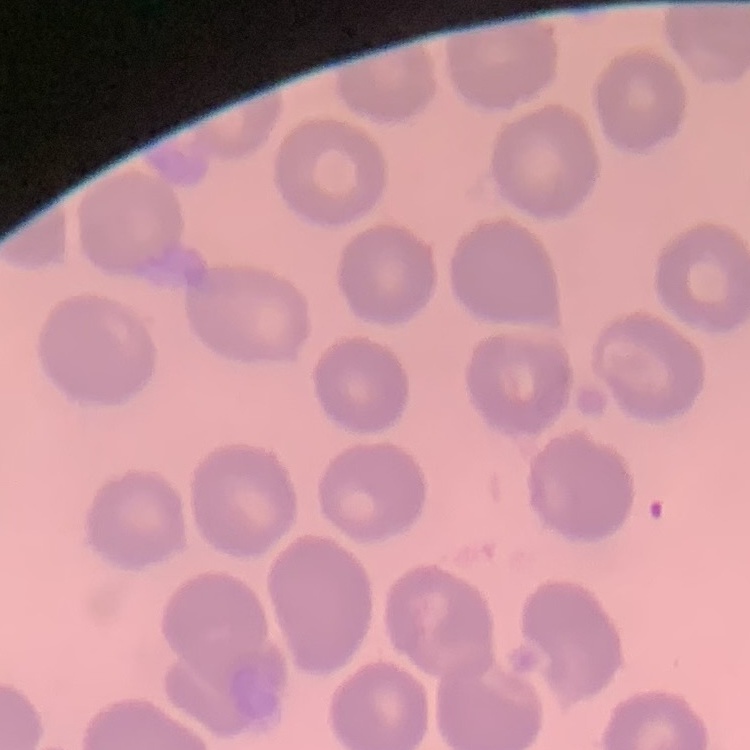

Summary:
  - Erythrocyte morphology: no rouleaux formation
  - Image type: one tile cut from a larger photomicrograph
  - Stain: Field's or Giemsa
  - Preparation: thin blood film